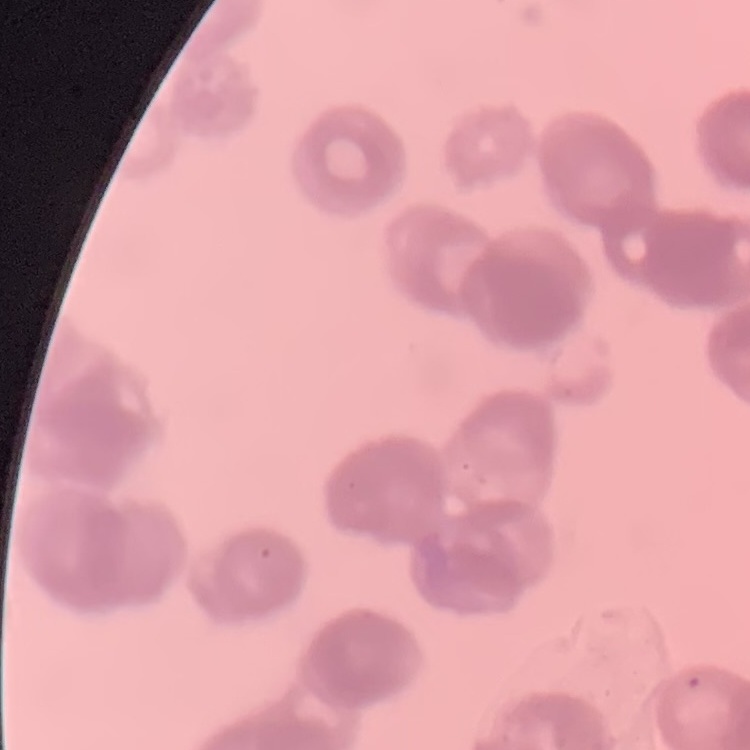

erythrocyte morphology = rouleaux formation
preparation = thin blood film
stain = Field's or Giemsa
image type = one tile cut from a larger photomicrograph